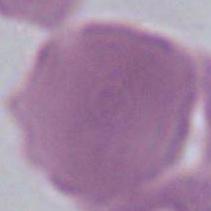
Captured at 1000x magnification. Micrograph. A red blood cell is shown.